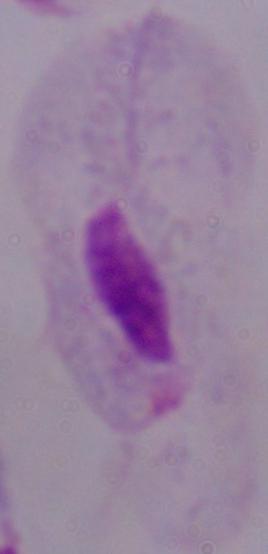
modality = photomicrograph
identification = trichomonad
magnification = 1000x